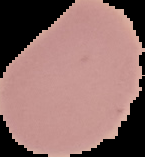
image_size: 145×157 pixels
preparation: thin blood film
image_type: cell region segmented out of the field of view; surrounding area masked to black
malaria_status: uninfected